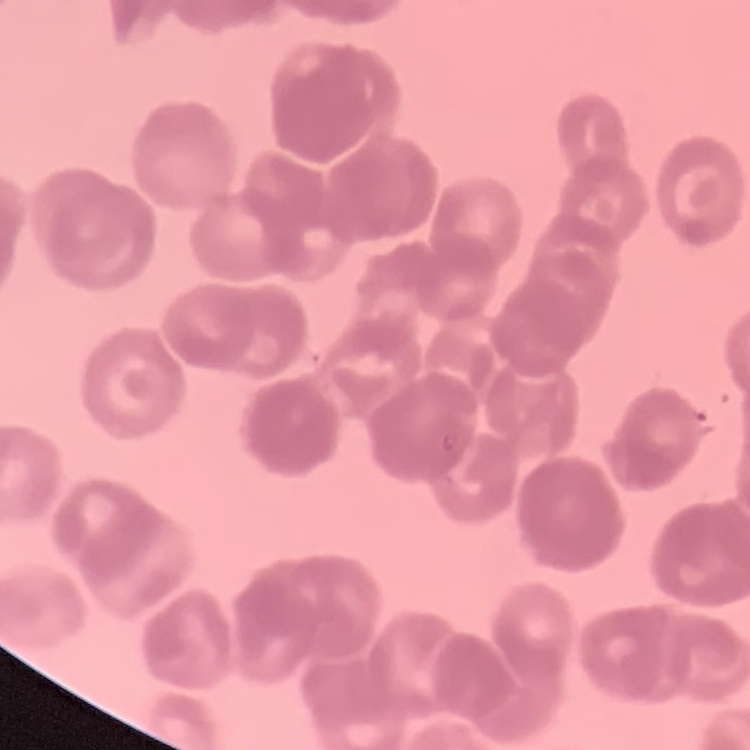 The erythrocytes exhibit rouleaux formation. Field's or Giemsa stain. Thin blood smear. Square crop of a larger photomicrograph.